Name the blood parasite species.
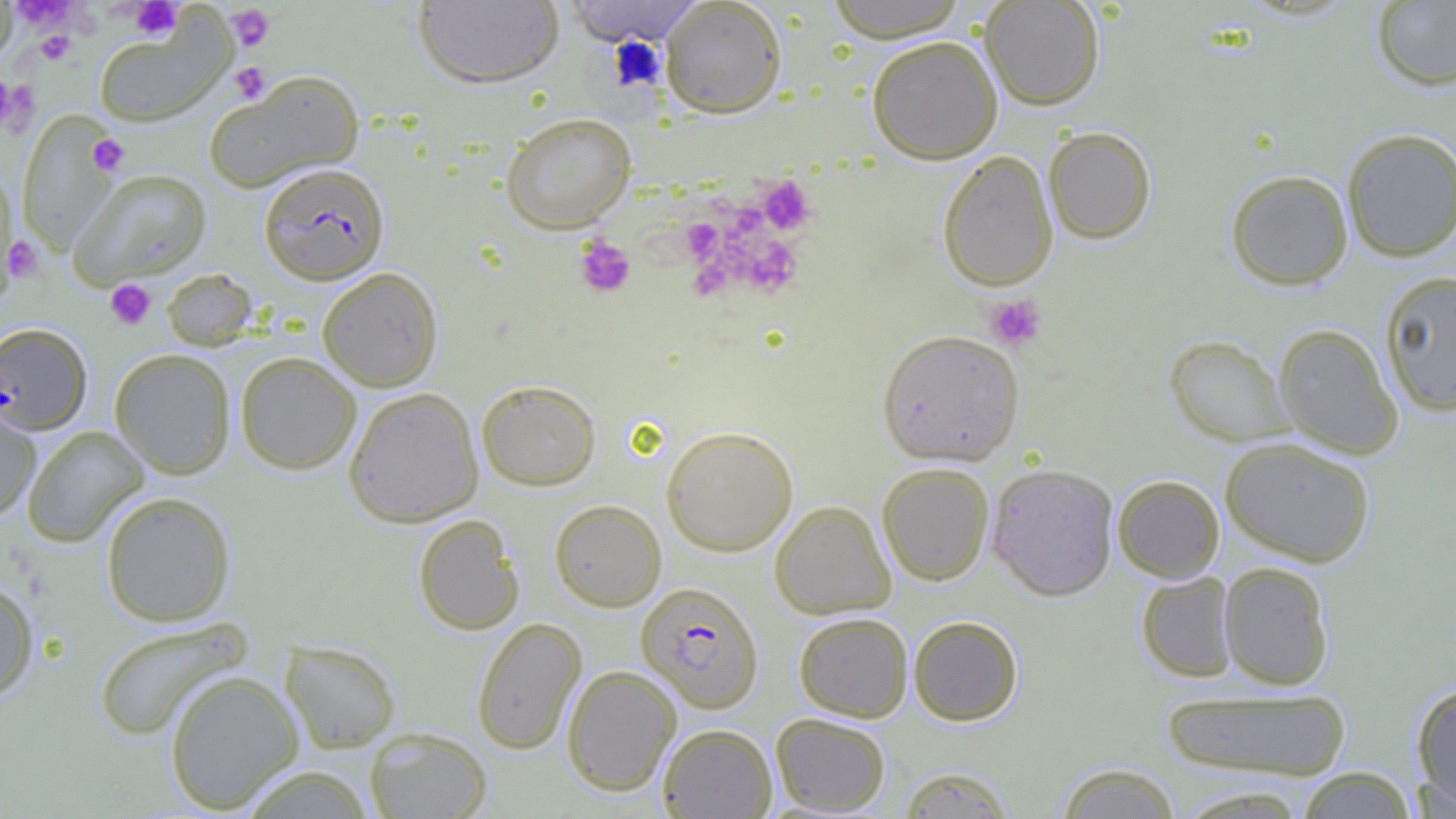
Plasmodium falciparum.

Approximate bounding boxes as [x1, y1, x2, y2] in pixels. Platelet locations: [12, 1, 78, 30], [128, 1, 182, 40], [226, 5, 275, 52], [36, 31, 75, 64], [608, 38, 667, 91], [229, 62, 271, 104], [0, 75, 16, 129], [0, 76, 40, 137], [88, 134, 129, 177], [757, 176, 815, 235], [731, 206, 761, 230], [682, 219, 723, 262], [4, 234, 44, 284], [735, 235, 803, 297], [574, 236, 636, 298], [696, 270, 732, 306], [105, 279, 156, 330], [984, 294, 1048, 351]. Uninfected red blood cell locations: [0, 0, 18, 66], [413, 0, 565, 88], [564, 0, 703, 46], [823, 0, 970, 42], [980, 0, 1105, 110], [660, 1, 787, 118], [1371, 1, 1456, 91], [93, 14, 236, 128], [866, 35, 1003, 164], [205, 69, 364, 192], [19, 112, 121, 255], [500, 112, 637, 233], [1043, 126, 1157, 244], [1340, 128, 1456, 262], [937, 150, 1058, 291], [0, 168, 19, 296], [68, 168, 212, 288], [1225, 169, 1353, 290], [317, 266, 444, 391], [162, 268, 259, 351], [1378, 269, 1456, 416], [1274, 323, 1404, 459], [877, 329, 1025, 466], [1164, 334, 1294, 446], [109, 348, 236, 480], [235, 351, 362, 475], [476, 379, 602, 491], [343, 387, 483, 528], [0, 398, 42, 521], [22, 425, 149, 548], [661, 425, 799, 556], [1220, 436, 1376, 567], [877, 462, 994, 586], [987, 463, 1119, 601], [1112, 474, 1225, 583], [100, 490, 236, 627], [549, 499, 666, 611], [770, 500, 896, 619], [413, 514, 524, 635], [1218, 560, 1335, 690], [1135, 571, 1238, 682], [0, 576, 39, 701], [793, 612, 913, 722], [908, 615, 1023, 726], [92, 616, 252, 742], [471, 617, 587, 755], [280, 640, 402, 754], [561, 664, 682, 796], [164, 670, 303, 813], [1411, 681, 1456, 811], [1160, 686, 1353, 781], [770, 712, 891, 815], [657, 723, 777, 818], [365, 726, 492, 819], [1053, 761, 1182, 819], [236, 764, 377, 819], [896, 765, 1016, 818], [1293, 766, 1420, 819], [1171, 785, 1311, 818]. Plasmodium falciparum-infected red blood cell locations: [258, 162, 389, 285], [0, 323, 93, 435], [636, 581, 764, 713]. Image is 1456×819 pixels. Thin blood smear. Light microscopy. Single field of view. 1000x magnification.